Assess this cell for malaria.
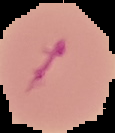

Parasitized.

{
  "preparation": "thin blood smear",
  "image_size": "115×133 pixels",
  "image_type": "cell region segmented out of the field of view; surrounding area masked to black"
}